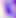

Photomicrograph. 400x magnification. Toxoplasma gondii is shown.